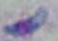 Captured at 1000x magnification. Toxoplasma gondii is seen. Photomicrograph.